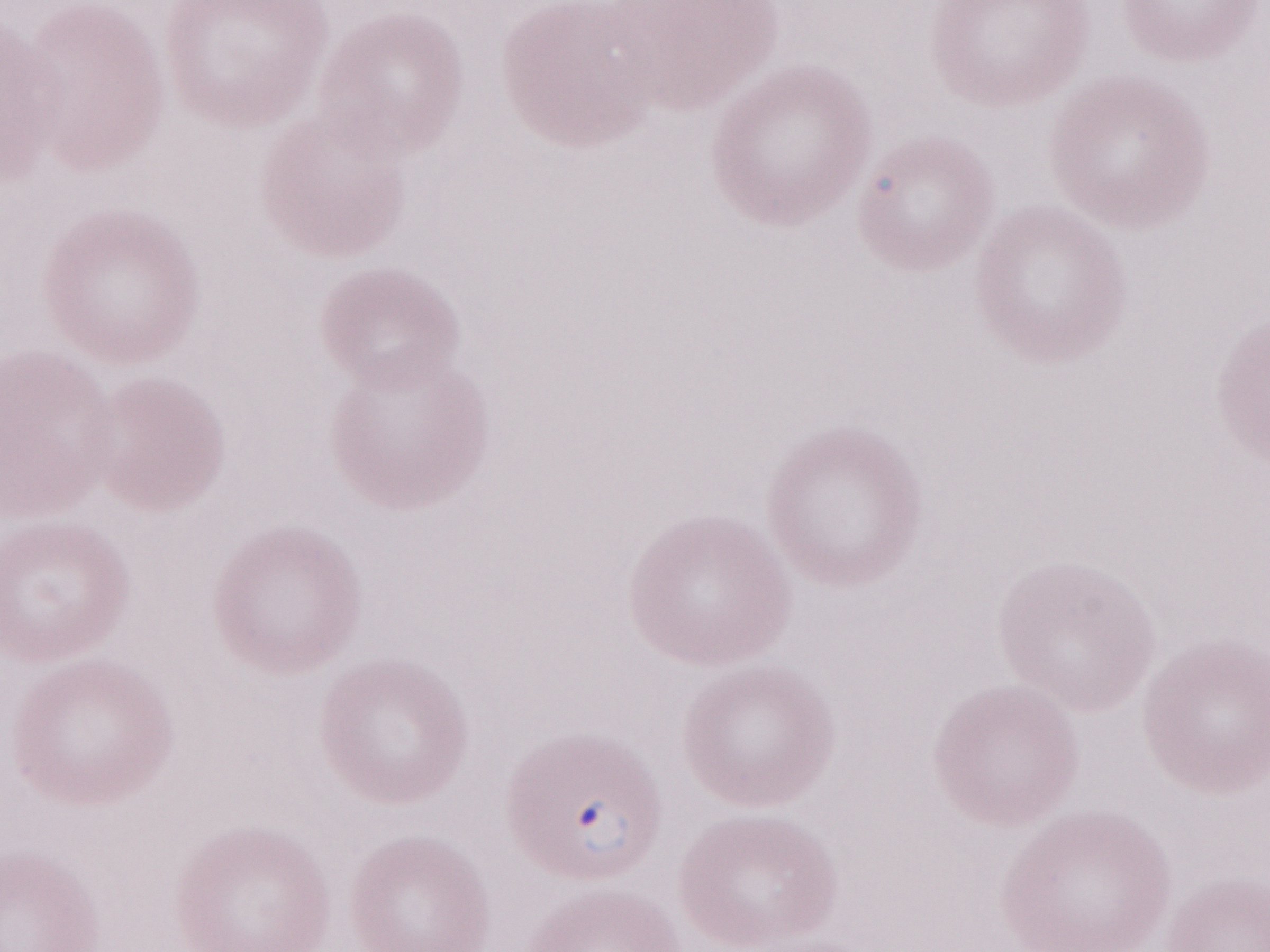 Malaria diagnosis (patient-level): positive. May-Grünwald-Giemsa (MGG) stain. Olympus BX43 microscope, Olympus DP73 camera. Image is 1270×952 pixels. Magnification: 1,000x. Thin blood film. One field of this slide.